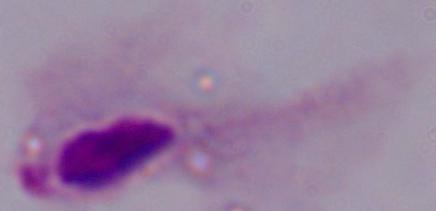

Summary:
  - Magnification: 1000x
  - Modality: micrograph
  - Identification: trichomonad